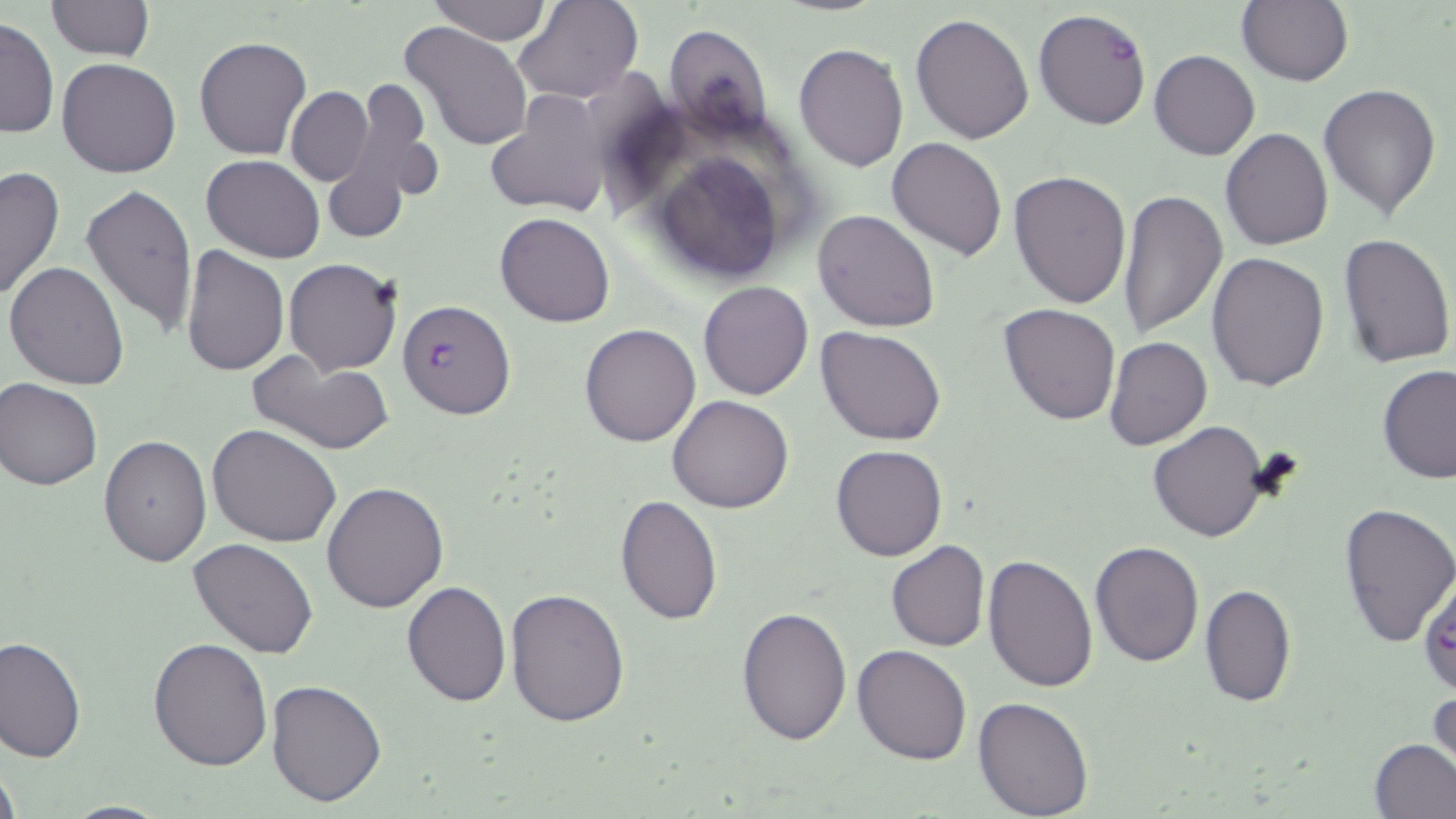

Summary:
  - Coordinate format: approximate bounding boxes as (x1, y1, x2, y2) in pixels
  - Plasmodium falciparum-infected red blood cell locations: (1033, 8, 1151, 130), (396, 299, 517, 420), (1417, 575, 1456, 699)
  - Uninfected red blood cell locations: (428, 0, 550, 45), (513, 0, 641, 103), (45, 1, 155, 62), (1235, 1, 1353, 87), (911, 12, 1034, 144), (1, 16, 58, 140), (398, 21, 533, 154), (663, 25, 772, 139), (793, 32, 1029, 156), (193, 35, 311, 159), (794, 43, 908, 174), (1149, 49, 1260, 160), (57, 57, 182, 178), (340, 76, 441, 219), (1318, 83, 1441, 220), (286, 88, 372, 184), (487, 90, 612, 221), (1219, 127, 1333, 251), (887, 135, 1008, 259), (641, 143, 793, 286), (201, 154, 325, 263), (0, 165, 65, 303), (1008, 169, 1131, 308), (80, 183, 199, 338), (1117, 187, 1227, 337), (813, 208, 941, 332), (495, 212, 615, 327), (1337, 233, 1455, 370), (179, 245, 289, 377), (1206, 252, 1330, 393), (283, 258, 402, 377), (6, 261, 129, 391), (698, 281, 814, 401), (998, 302, 1122, 425), (579, 323, 702, 447), (816, 325, 947, 445), (1104, 337, 1213, 451), (244, 347, 396, 456), (1378, 363, 1456, 485), (0, 377, 102, 490), (667, 394, 795, 512), (1148, 420, 1269, 541), (207, 423, 341, 549), (98, 434, 211, 567), (831, 444, 948, 562), (322, 481, 450, 613), (613, 495, 724, 625), (1338, 501, 1456, 649), (187, 538, 319, 658), (1089, 539, 1207, 668), (886, 540, 989, 653), (983, 553, 1100, 692), (402, 580, 512, 707), (1200, 583, 1294, 708), (506, 588, 632, 727), (736, 605, 852, 746), (0, 633, 85, 762), (148, 638, 273, 771), (851, 643, 973, 764), (265, 677, 388, 807), (1427, 689, 1454, 776), (972, 696, 1096, 817), (1370, 738, 1456, 818), (0, 758, 21, 819), (59, 800, 178, 818)
  - Slide-level diagnosis: Plasmodium falciparum
  - Image size: 1456×819 pixels
  - Stain: May-Grünwald-Giemsa
  - Modality: optical microscopy
  - Field of view: one of a larger specimen
  - Magnification: 1000x
  - Preparation: thin blood film